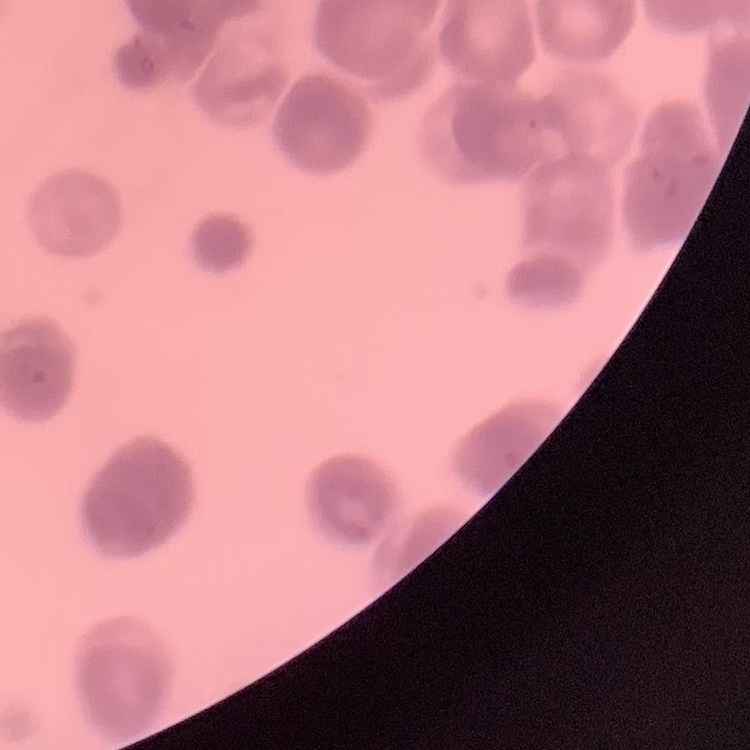
Summary:
  - Red blood cell morphology: rouleaux formation
  - Preparation: thin blood smear
  - Stain: Field's or Giemsa
  - Image type: one tile cut from a larger photomicrograph